Name the parasite shown.
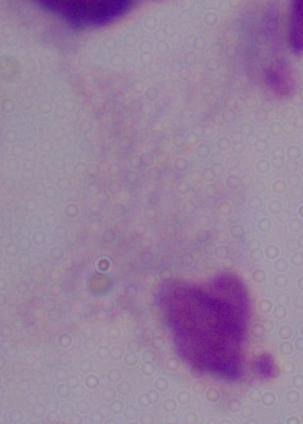
A trichomonad.

1000x magnification. Micrograph.